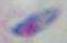 1000x magnification. Photomicrograph. Toxoplasma gondii is seen.